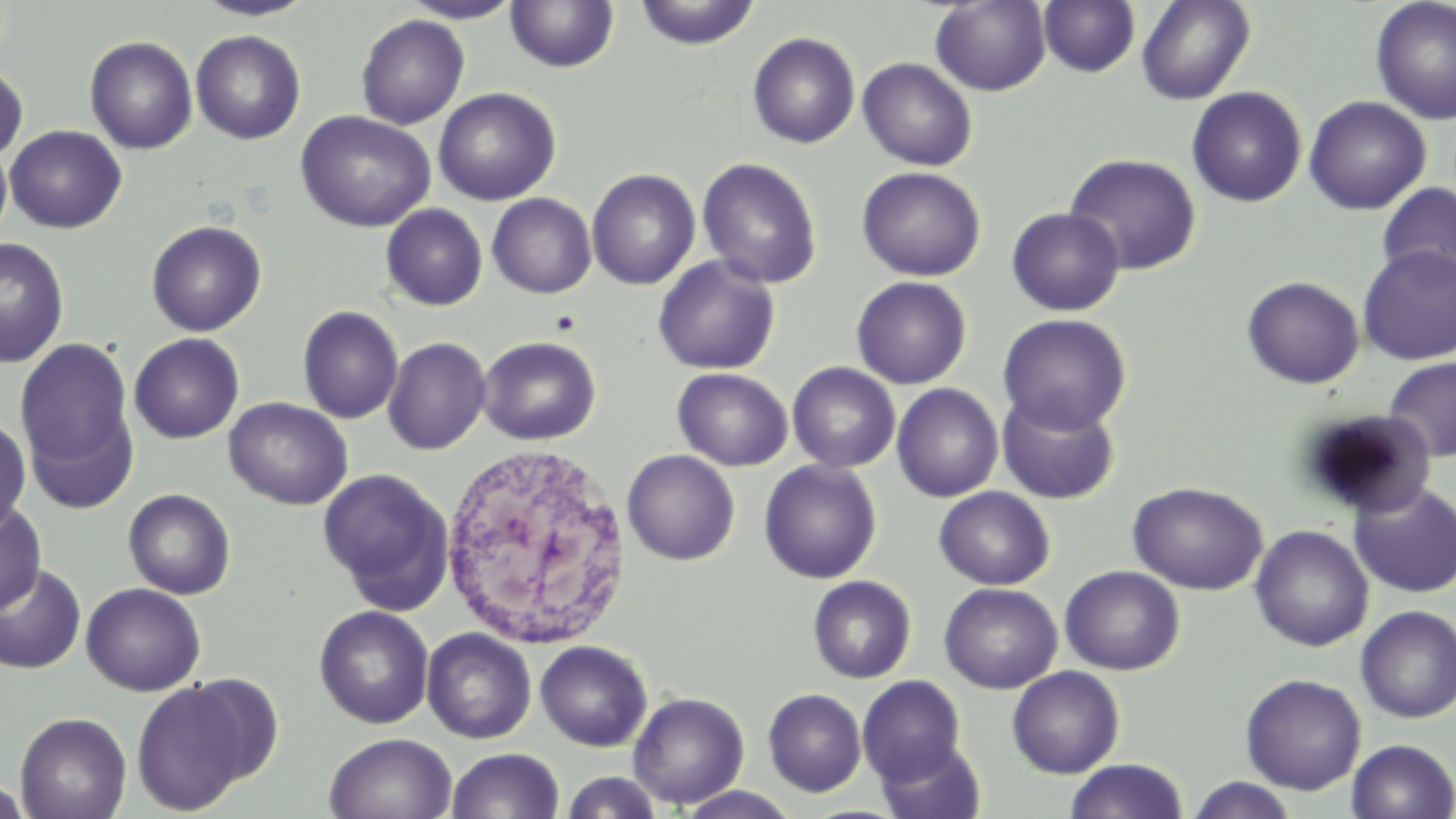 Approximate bounding boxes as named x1/y1/x2/y2 corners in pixels. Uninfected red blood cell locations: (x1=193, y1=0, x2=318, y2=21), (x1=400, y1=0, x2=523, y2=23), (x1=929, y1=0, x2=1051, y2=95), (x1=1136, y1=0, x2=1255, y2=104), (x1=1370, y1=0, x2=1456, y2=125), (x1=633, y1=1, x2=761, y2=50), (x1=1038, y1=1, x2=1141, y2=78), (x1=505, y1=2, x2=620, y2=74), (x1=356, y1=14, x2=469, y2=129), (x1=191, y1=30, x2=306, y2=144), (x1=748, y1=32, x2=860, y2=148), (x1=84, y1=35, x2=198, y2=154), (x1=857, y1=58, x2=977, y2=171), (x1=0, y1=64, x2=28, y2=164), (x1=1186, y1=86, x2=1307, y2=207), (x1=433, y1=87, x2=561, y2=205), (x1=1304, y1=95, x2=1431, y2=215), (x1=295, y1=110, x2=436, y2=232), (x1=1347, y1=116, x2=1452, y2=271), (x1=5, y1=125, x2=127, y2=233), (x1=0, y1=139, x2=12, y2=243), (x1=1063, y1=152, x2=1201, y2=275), (x1=698, y1=157, x2=822, y2=289), (x1=857, y1=166, x2=985, y2=281), (x1=586, y1=168, x2=700, y2=290), (x1=1376, y1=182, x2=1456, y2=288), (x1=487, y1=193, x2=597, y2=298), (x1=381, y1=204, x2=488, y2=311), (x1=1006, y1=207, x2=1125, y2=316), (x1=146, y1=220, x2=267, y2=336), (x1=0, y1=238, x2=70, y2=369), (x1=1358, y1=245, x2=1456, y2=364), (x1=653, y1=256, x2=780, y2=375), (x1=851, y1=275, x2=972, y2=389), (x1=1242, y1=276, x2=1365, y2=389), (x1=298, y1=305, x2=403, y2=424), (x1=997, y1=313, x2=1132, y2=435), (x1=129, y1=333, x2=244, y2=443), (x1=15, y1=336, x2=135, y2=484), (x1=477, y1=336, x2=601, y2=445), (x1=383, y1=337, x2=491, y2=455), (x1=1382, y1=357, x2=1456, y2=462), (x1=787, y1=362, x2=901, y2=473), (x1=672, y1=368, x2=793, y2=471), (x1=892, y1=383, x2=1004, y2=502), (x1=996, y1=392, x2=1120, y2=505), (x1=224, y1=397, x2=353, y2=510), (x1=1300, y1=409, x2=1437, y2=519), (x1=0, y1=416, x2=31, y2=533), (x1=622, y1=449, x2=740, y2=565), (x1=759, y1=459, x2=882, y2=584), (x1=317, y1=468, x2=454, y2=611), (x1=1128, y1=481, x2=1268, y2=594), (x1=1350, y1=483, x2=1456, y2=597), (x1=934, y1=487, x2=1055, y2=589), (x1=123, y1=488, x2=236, y2=599), (x1=0, y1=498, x2=46, y2=617), (x1=1250, y1=525, x2=1374, y2=652), (x1=0, y1=563, x2=86, y2=674), (x1=1060, y1=565, x2=1185, y2=675), (x1=0, y1=569, x2=169, y2=686), (x1=808, y1=576, x2=915, y2=683), (x1=81, y1=583, x2=206, y2=696), (x1=939, y1=583, x2=1062, y2=693), (x1=314, y1=605, x2=434, y2=728), (x1=1355, y1=605, x2=1456, y2=723), (x1=422, y1=628, x2=536, y2=744), (x1=535, y1=640, x2=652, y2=751), (x1=1007, y1=666, x2=1125, y2=778), (x1=1240, y1=673, x2=1366, y2=794), (x1=857, y1=675, x2=966, y2=784), (x1=131, y1=678, x2=257, y2=815), (x1=763, y1=688, x2=866, y2=796), (x1=628, y1=692, x2=749, y2=809), (x1=15, y1=711, x2=132, y2=819), (x1=324, y1=732, x2=457, y2=819), (x1=875, y1=738, x2=986, y2=819), (x1=1346, y1=739, x2=1456, y2=818), (x1=446, y1=748, x2=564, y2=819), (x1=1063, y1=759, x2=1189, y2=819), (x1=0, y1=769, x2=30, y2=818), (x1=561, y1=771, x2=663, y2=818), (x1=1185, y1=776, x2=1298, y2=818), (x1=671, y1=786, x2=803, y2=818). White blood cell locations: (x1=437, y1=442, x2=634, y2=652). Slide-level diagnosis: negative for blood parasites. Image is 1456×819 pixels. Captured at 1000x magnification. May-Grünwald-Giemsa stain. One field of a larger specimen. Thin blood smear. Light microscopy.